Identify the parasite.
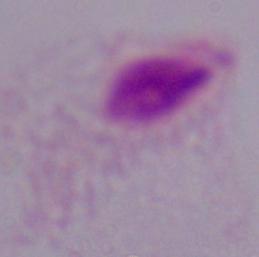

This is a trichomonad.

magnification: 1000x
modality: photomicrograph